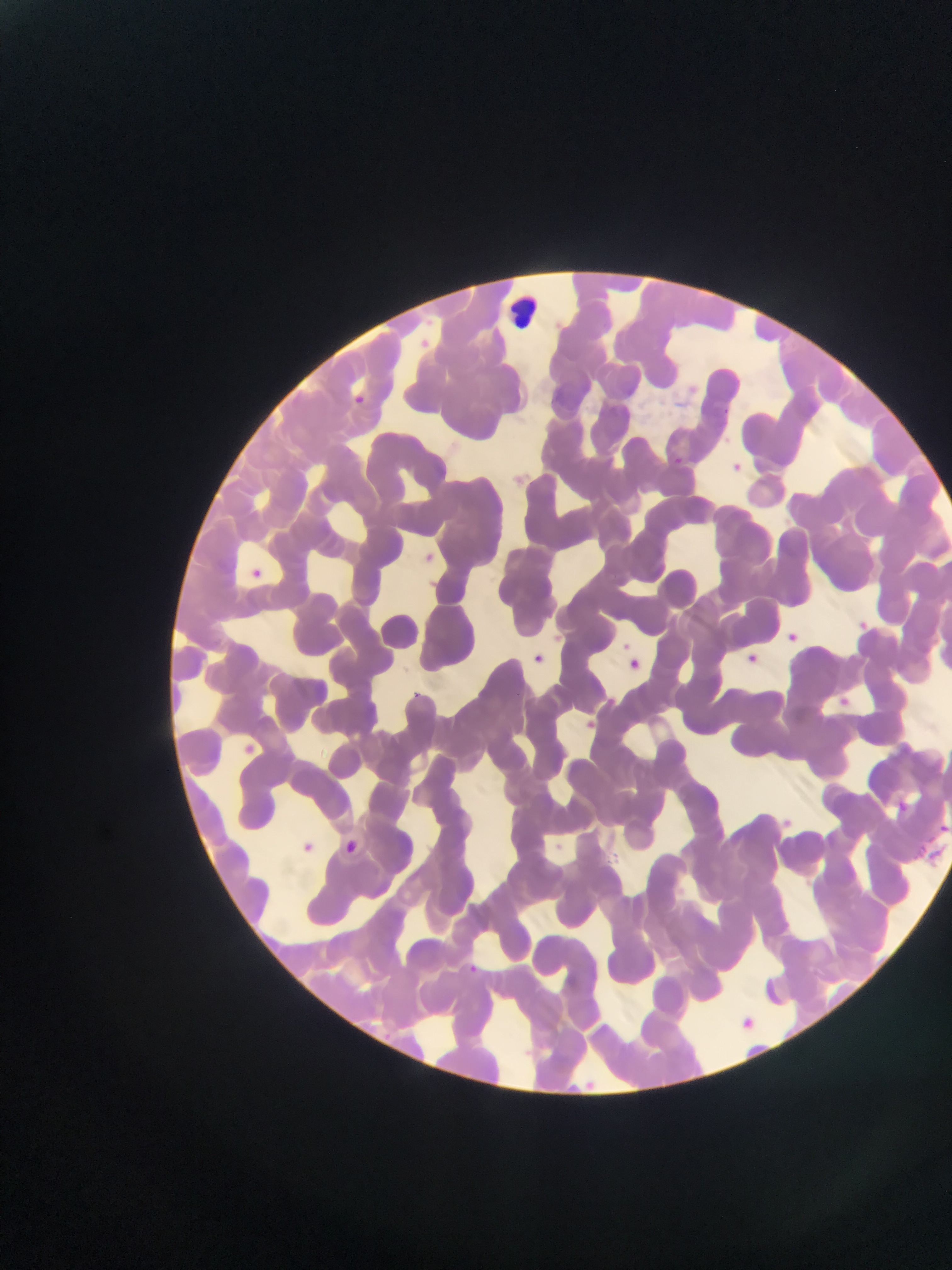
Approximate bounding boxes as (left, top, right, bottom) in pixels. Leukocyte locations: (493, 278, 556, 352). Plasmodium parasite locations: (398, 324, 451, 358), (720, 386, 749, 417), (350, 389, 379, 419), (667, 444, 694, 475), (731, 458, 748, 481), (421, 543, 446, 573), (250, 567, 271, 583), (860, 613, 874, 636), (785, 630, 805, 646), (529, 644, 551, 669), (748, 646, 762, 666), (626, 657, 644, 673), (404, 685, 439, 717), (836, 692, 850, 711), (582, 716, 602, 732), (238, 731, 271, 772), (896, 793, 926, 824), (936, 813, 952, 833), (347, 834, 368, 861), (304, 838, 328, 856), (913, 844, 943, 861), (464, 960, 481, 976), (739, 1008, 759, 1036), (583, 1073, 600, 1097). One field of view. Collected in Ghana. Thin blood smear. Image is 952×1270 pixels. Photographed through a microscope with a mobile-phone camera.